Identify the parasite.
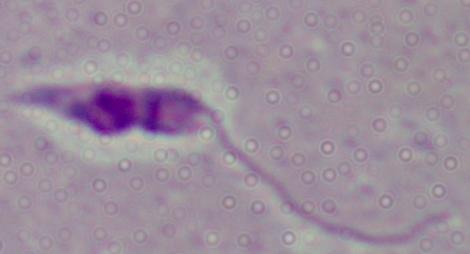

This is Leishmania.

Summary:
  - Modality: photomicrograph
  - Magnification: 1000x